Name the blood parasite species.
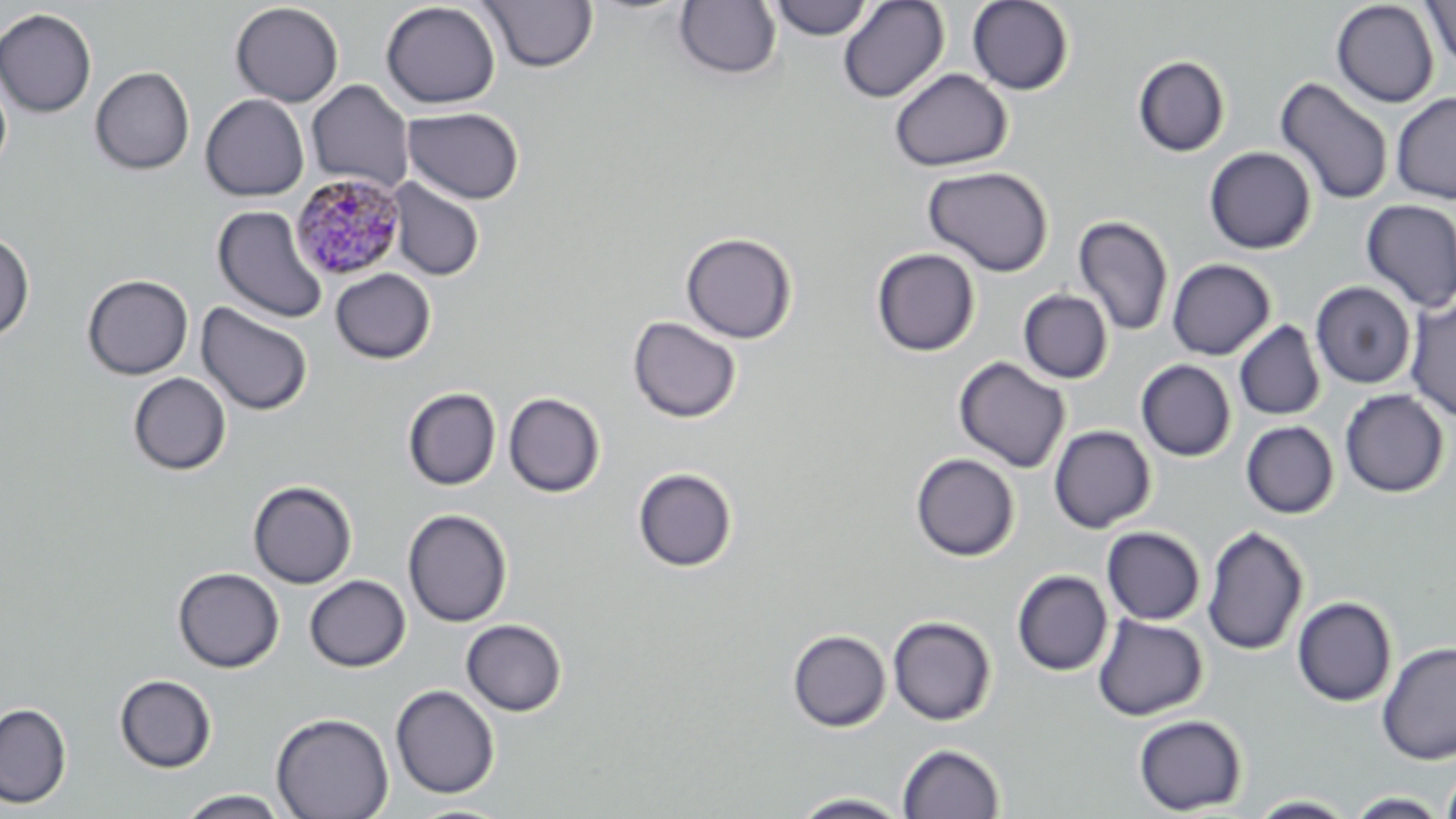

Plasmodium malariae.

Summary:
  - Coordinate format: approximate bounding boxes as [x1, y1, x2, y2] in pixels
  - Plasmodium malariae-infected red blood cell locations: [289, 172, 407, 281]
  - Uninfected red blood cell locations: [478, 0, 598, 73], [768, 0, 874, 40], [837, 0, 949, 103], [380, 1, 502, 109], [673, 1, 782, 80], [967, 1, 1074, 95], [1331, 1, 1439, 108], [1421, 1, 1456, 68], [230, 2, 344, 107], [0, 8, 97, 117], [1132, 55, 1230, 157], [90, 66, 195, 175], [889, 69, 1013, 172], [0, 74, 12, 176], [1275, 77, 1394, 205], [306, 80, 415, 193], [1391, 92, 1456, 204], [200, 94, 309, 201], [402, 106, 525, 203], [1204, 146, 1316, 254], [923, 165, 1054, 277], [387, 177, 485, 281], [1360, 199, 1456, 313], [212, 206, 328, 324], [1073, 215, 1174, 337], [0, 230, 35, 343], [681, 232, 797, 343], [871, 248, 981, 357], [1167, 258, 1275, 360], [330, 268, 436, 364], [82, 274, 194, 380], [1311, 281, 1416, 389], [1018, 289, 1114, 384], [1404, 299, 1456, 422], [195, 302, 314, 416], [627, 316, 742, 424], [1234, 320, 1326, 421], [953, 356, 1071, 473], [1136, 359, 1236, 462], [127, 372, 232, 475], [403, 387, 501, 490], [1340, 389, 1450, 497], [503, 392, 606, 498], [1240, 420, 1339, 518], [1049, 425, 1156, 533], [910, 453, 1020, 561], [632, 467, 738, 572], [248, 480, 357, 589], [403, 508, 513, 628], [1201, 524, 1309, 656], [1102, 526, 1206, 625], [173, 567, 284, 672], [1012, 570, 1113, 676], [305, 574, 411, 672], [1292, 596, 1397, 706], [1093, 614, 1208, 721], [888, 615, 997, 725], [461, 619, 567, 716], [787, 629, 891, 732], [1377, 641, 1456, 764], [114, 674, 217, 773], [390, 684, 500, 798], [0, 703, 72, 808], [271, 712, 394, 819], [1133, 714, 1248, 815], [897, 742, 1005, 819], [1440, 763, 1456, 819], [176, 789, 291, 818], [790, 791, 912, 818], [1344, 792, 1449, 818], [1246, 795, 1359, 818], [404, 802, 516, 818]
  - Modality: light microscopy
  - Magnification: 1000x
  - Field of view: single
  - Preparation: thin blood film
  - Image size: 1456×819 pixels
  - Stain: May-Grünwald-Giemsa